Describe the morphology of the red blood cells.
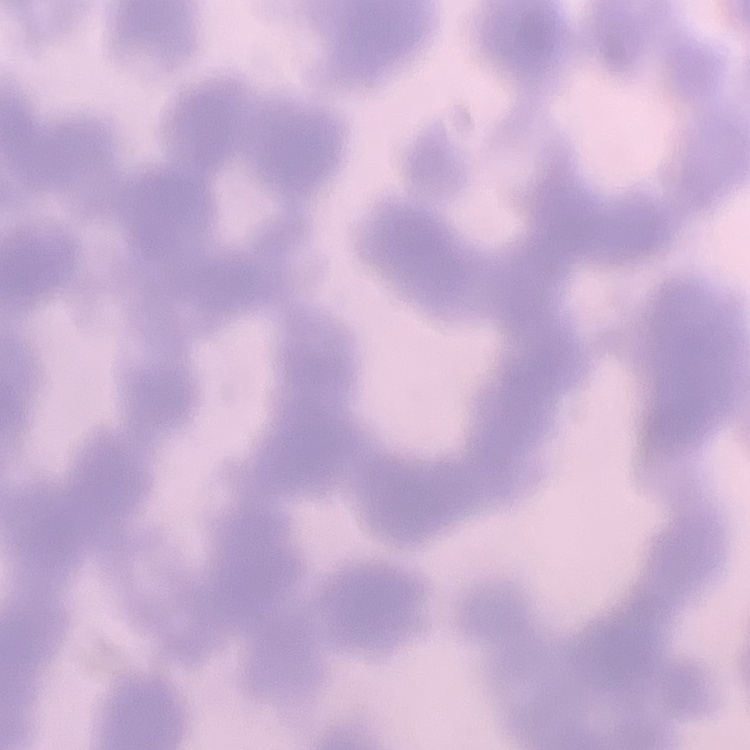

They show rouleaux formation.

Field's or Giemsa stain. Square crop of a larger photomicrograph. Thin blood smear.